Classify the preparation.
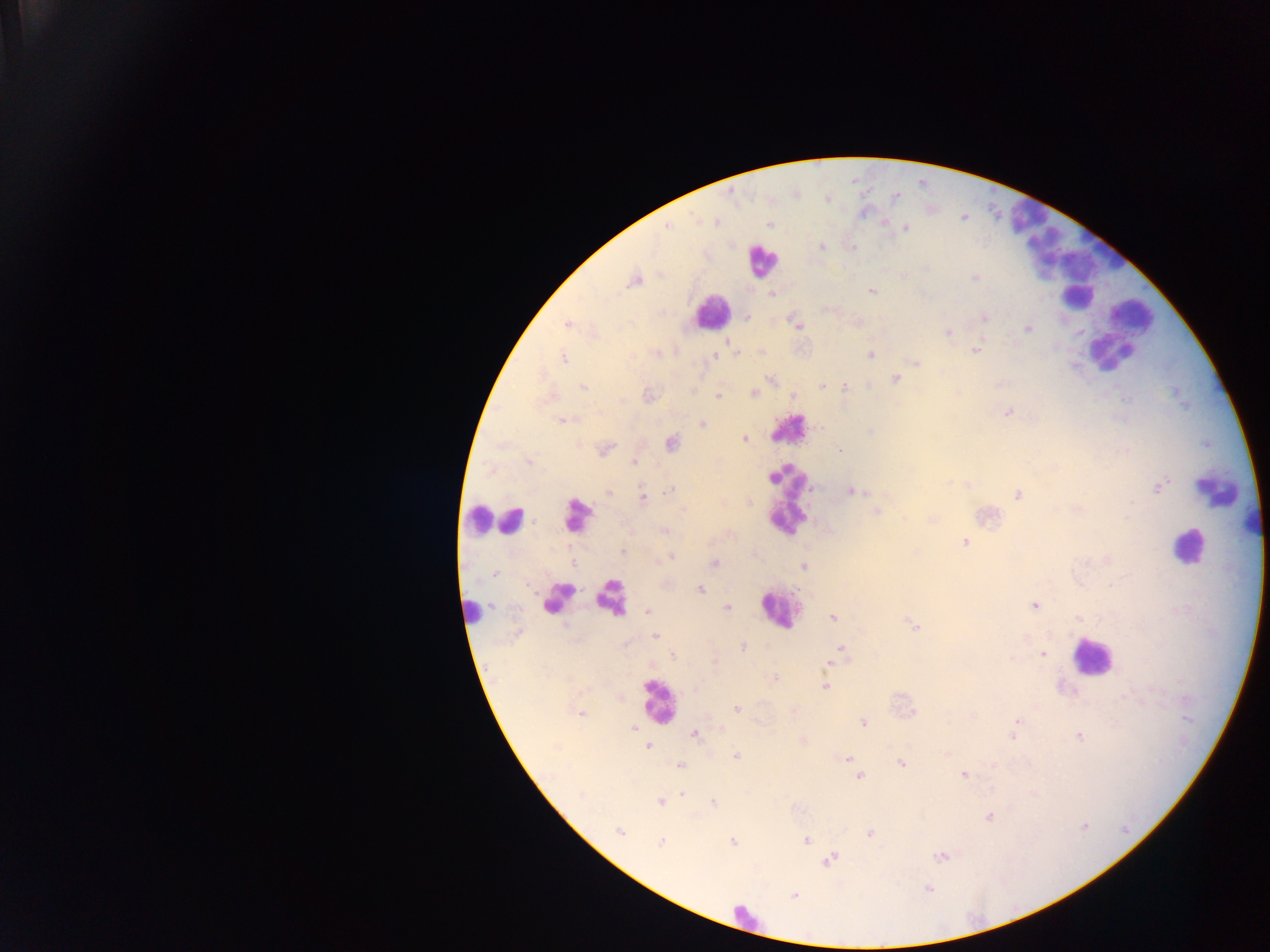
Thick blood film.

Approximate centers as x y in pixels. Leukocyte locations: 760 260; 1078 301; 1129 312; 709 313; 1103 351; 790 428; 1214 490; 472 519; 512 519; 1191 548; 780 613; 1096 658; 660 699. Plasmodium parasite locations: 893 199; 862 213; 716 221; 884 222; 668 226; 907 228; 823 247; 853 249; 925 267; 975 278; 635 281; 870 290; 985 319; 567 324; 797 327; 1026 329; 947 332; 976 349; 722 351; 657 353; 869 354; 713 357; 564 358; 915 361; 894 378; 820 384; 827 386; 583 387; 846 387; 694 389; 753 392; 648 394; 792 394; 717 395; 1008 412; 560 420; 703 422; 743 438; 671 443; 839 449; 604 450; 528 463; 634 463; 773 477; 948 481; 967 483; 1159 486; 809 488; 607 490; 668 490; 851 490; 858 492; 1017 494; 642 497; 749 502; 1133 505; 577 509; 1075 509; 876 511; 573 517; 1126 519; 931 520; 665 531; 964 543; 622 550; 671 556; 1105 559; 1083 562; 464 563; 573 563; 715 563; 803 566; 496 576; 700 590; 608 597; 493 606; 552 606; 1036 606; 728 607; 471 611; 649 612; 832 616; 1077 618; 912 626; 655 636; 1026 637; 741 646; 840 648; 1044 654; 671 655; 714 662; 827 666; 647 685; 825 686; 1127 697; 736 708; 581 712; 1186 717; 863 723; 1017 724; 633 727; 1013 733; 693 736; 1079 736; 647 747; 736 756; 846 757; 901 763; 680 766; 964 773; 860 776; 684 794; 660 802; 713 802; 795 807; 989 816; 1084 828; 620 832; 870 833; 807 841; 662 842; 733 842; 941 856; 833 858; 829 861; 928 890; 795 895. Collected in Ghana. One field of view. Photographed through a microscope with a mobile-phone camera. Image is 1270×952 pixels.